Name the blood parasite species.
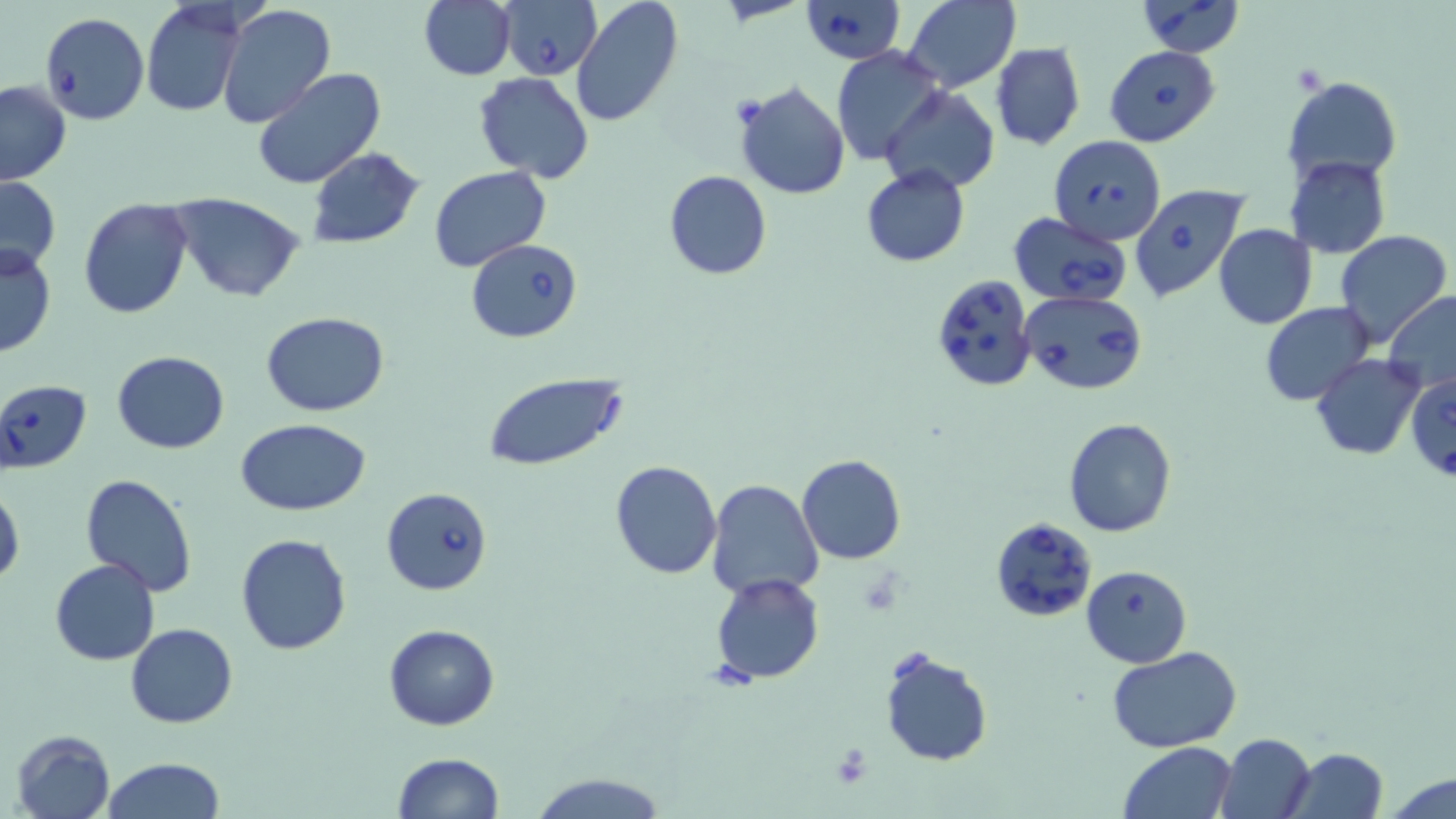

Babesia divergens.

Approximate bounding boxes as (x1, y1, x2, y2) in pixels. Uninfected red blood cell locations: (420, 0, 515, 81), (570, 0, 685, 127), (903, 0, 1021, 92), (140, 4, 248, 118), (216, 4, 336, 127), (989, 43, 1085, 151), (831, 46, 947, 166), (253, 68, 385, 189), (474, 73, 595, 184), (1282, 75, 1402, 183), (735, 80, 852, 201), (0, 81, 72, 186), (883, 88, 999, 194), (305, 147, 425, 248), (1284, 156, 1390, 258), (429, 166, 551, 274), (861, 166, 970, 266), (664, 170, 770, 280), (0, 177, 61, 276), (171, 196, 306, 303), (79, 197, 193, 319), (1213, 224, 1317, 330), (1334, 228, 1452, 347), (0, 242, 56, 359), (1382, 291, 1456, 401), (1261, 301, 1376, 405), (261, 312, 389, 417), (112, 350, 230, 455), (1310, 354, 1426, 460), (482, 375, 629, 469), (1064, 417, 1176, 538), (236, 419, 372, 515), (797, 454, 906, 565), (609, 461, 723, 581), (80, 472, 198, 595), (705, 479, 824, 601), (0, 481, 24, 587), (234, 532, 352, 655), (50, 559, 160, 666), (1080, 564, 1190, 667), (711, 573, 823, 685), (126, 623, 236, 728), (383, 623, 500, 730), (879, 647, 992, 766), (1107, 647, 1244, 750), (11, 728, 115, 819), (1216, 733, 1316, 819), (1119, 741, 1236, 819), (1288, 748, 1389, 818), (392, 751, 505, 819), (102, 757, 225, 819), (528, 771, 670, 818), (1386, 773, 1455, 819). Platelet locations: (830, 742, 873, 788). Babesia divergens-infected red blood cell locations: (797, 0, 905, 63), (1135, 0, 1244, 56), (499, 1, 601, 81), (39, 13, 149, 125), (1105, 45, 1220, 147), (1049, 135, 1166, 244), (1129, 184, 1247, 302), (1010, 212, 1131, 308), (469, 239, 583, 343), (931, 273, 1040, 392), (1019, 289, 1147, 394), (1409, 368, 1456, 487), (0, 379, 94, 474), (382, 487, 492, 595), (989, 517, 1097, 623). Image is 1456×819 pixels. Single field of view. 1000x magnification. Thin blood film. Light microscopy. May-Grünwald-Giemsa-stained preparation.